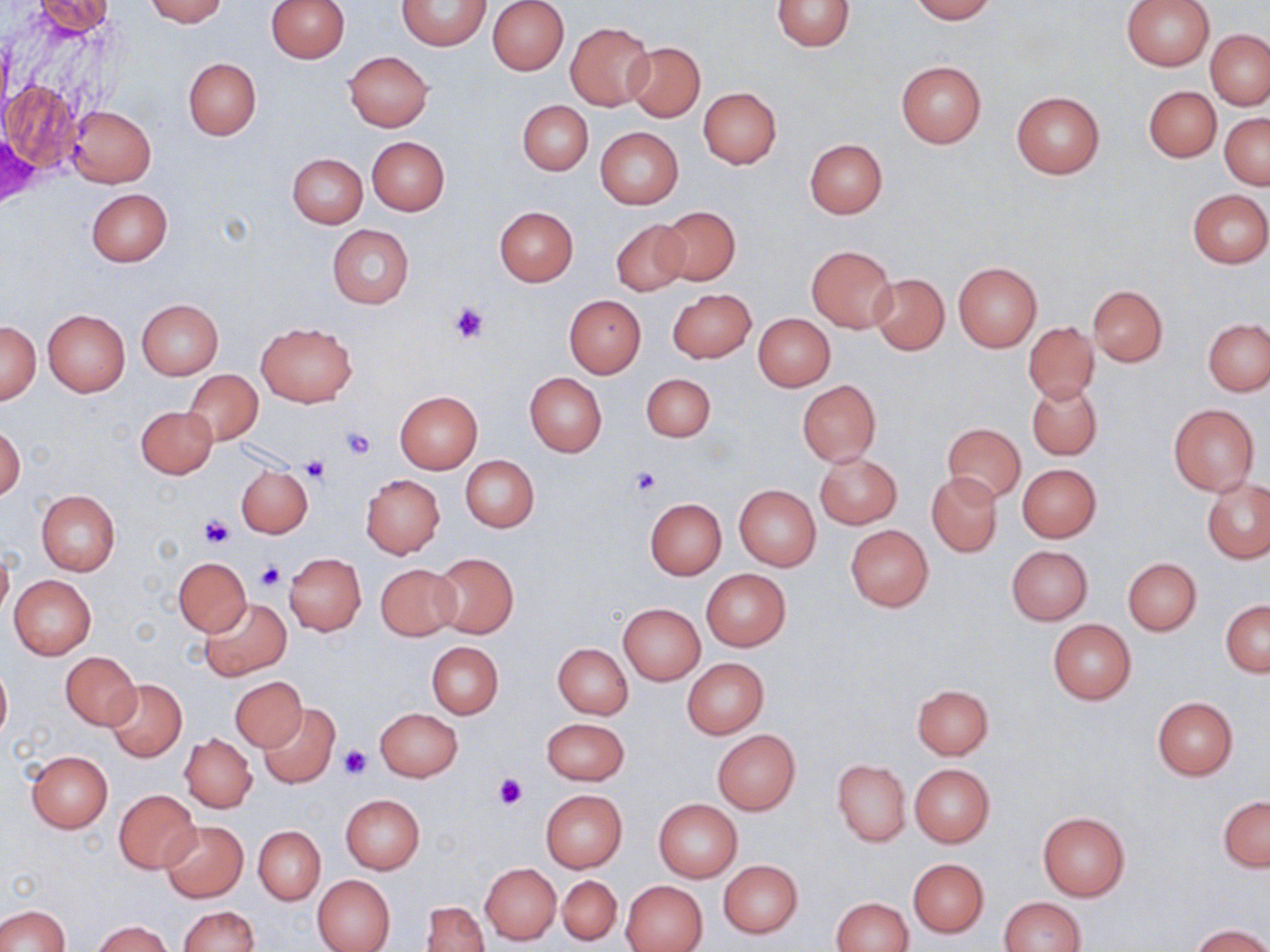

Approximate bounding boxes as [x1, y1, x2, y2] in pixels. Platelet locations: [450, 301, 491, 346], [341, 426, 376, 460], [300, 456, 330, 485], [630, 466, 663, 495], [201, 515, 235, 549], [254, 561, 284, 591], [339, 745, 371, 779], [494, 772, 526, 809]. Uninfected red blood cell locations: [31, 0, 116, 39], [145, 0, 227, 25], [264, 0, 349, 63], [488, 0, 568, 75], [771, 0, 855, 50], [910, 0, 996, 23], [1121, 0, 1215, 70], [397, 1, 491, 50], [565, 22, 654, 110], [1206, 30, 1270, 110], [625, 43, 705, 121], [343, 51, 432, 131], [183, 58, 260, 139], [895, 61, 986, 147], [3, 80, 82, 173], [1144, 86, 1220, 162], [698, 87, 781, 168], [1011, 91, 1105, 177], [518, 100, 593, 175], [66, 105, 156, 187], [1221, 113, 1269, 190], [595, 127, 683, 208], [367, 137, 449, 215], [804, 139, 887, 219], [287, 153, 367, 227], [86, 188, 172, 266], [1187, 189, 1270, 267], [494, 206, 578, 285], [656, 206, 740, 286], [610, 219, 689, 297], [328, 225, 414, 309], [806, 246, 897, 331], [953, 262, 1041, 351], [870, 273, 949, 355], [1087, 284, 1168, 366], [667, 289, 756, 363], [564, 295, 646, 377], [135, 298, 223, 379], [43, 309, 130, 395], [754, 314, 835, 391], [1203, 318, 1270, 396], [0, 322, 41, 403], [256, 322, 356, 406], [1023, 322, 1098, 403], [183, 371, 263, 446], [641, 373, 714, 442], [525, 374, 607, 455], [797, 380, 881, 465], [1026, 380, 1102, 461], [395, 391, 482, 473], [1167, 402, 1260, 496], [137, 405, 218, 478], [943, 424, 1026, 503], [1, 425, 24, 503], [814, 453, 901, 529], [461, 456, 538, 532], [1017, 463, 1101, 542], [235, 465, 313, 538], [926, 472, 1003, 556], [360, 474, 445, 558], [1202, 477, 1270, 563], [734, 485, 821, 572], [36, 490, 121, 576], [645, 498, 726, 579], [846, 526, 933, 611], [1007, 546, 1092, 624], [0, 548, 13, 623], [285, 552, 366, 635], [429, 552, 519, 639], [173, 557, 252, 636], [1123, 558, 1202, 636], [375, 563, 460, 640], [701, 569, 791, 650], [9, 574, 96, 659], [201, 598, 292, 680], [1221, 600, 1270, 675], [618, 603, 705, 684], [1047, 619, 1137, 705], [427, 641, 504, 718], [554, 643, 633, 719], [60, 652, 140, 729], [682, 657, 769, 738], [0, 662, 11, 743], [231, 677, 306, 751], [106, 678, 186, 761], [912, 684, 994, 759], [1151, 696, 1239, 779], [257, 703, 341, 788], [375, 707, 463, 782], [541, 717, 630, 785], [713, 730, 800, 814], [181, 734, 257, 812], [26, 751, 113, 832], [831, 759, 910, 846], [909, 764, 995, 847], [114, 789, 200, 874], [541, 790, 627, 872], [340, 795, 425, 874], [1219, 795, 1270, 872], [654, 800, 742, 881], [1038, 812, 1129, 900], [159, 820, 248, 903], [253, 825, 325, 904], [909, 858, 989, 937], [719, 860, 803, 937], [481, 863, 561, 945], [312, 874, 395, 952], [557, 875, 621, 946], [620, 880, 707, 951], [830, 897, 912, 951], [998, 897, 1085, 952], [422, 901, 489, 951], [0, 905, 70, 952], [177, 905, 258, 952], [91, 920, 172, 952], [1190, 924, 1269, 952]. Slide-level diagnosis: negative for blood parasites. Single field of view. Image is 1270×952 pixels. Thin blood film. Light microscopy. Captured at 1000x magnification. May-Grünwald-Giemsa stain.